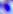
identification: Toxoplasma gondii
magnification: 400x
modality: micrograph